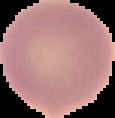
From a thin blood film. Image is 115×118 pixels. Malaria status: uninfected. Cell region segmented out of the field of view; the surrounding area is masked to black.